Assess the morphology of the erythrocytes.
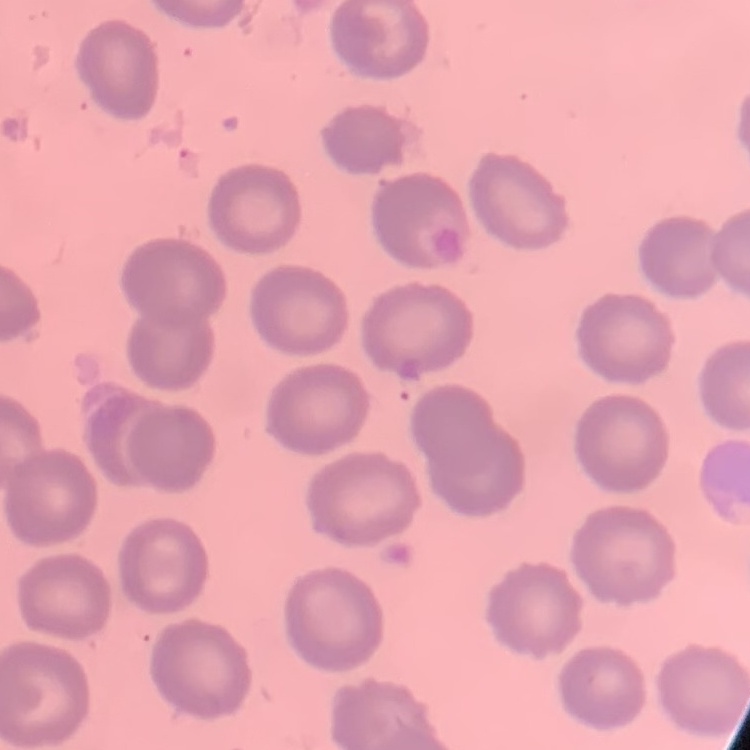
They show no rouleaux formation.

Thin blood film. Square crop of a larger photomicrograph. Stained with either Field's or Giemsa.